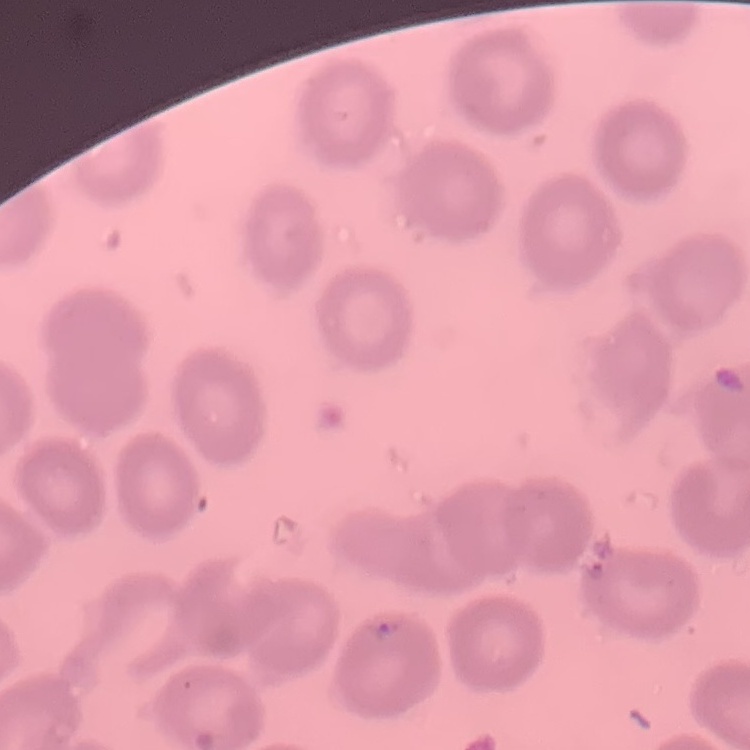

Summary:
  - Erythrocyte morphology: no rouleaux formation
  - Stain: Field's or Giemsa
  - Image type: one tile cut from a larger photomicrograph
  - Preparation: thin peripheral smear